Locate every Plasmodium falciparum-infected red blood cell.
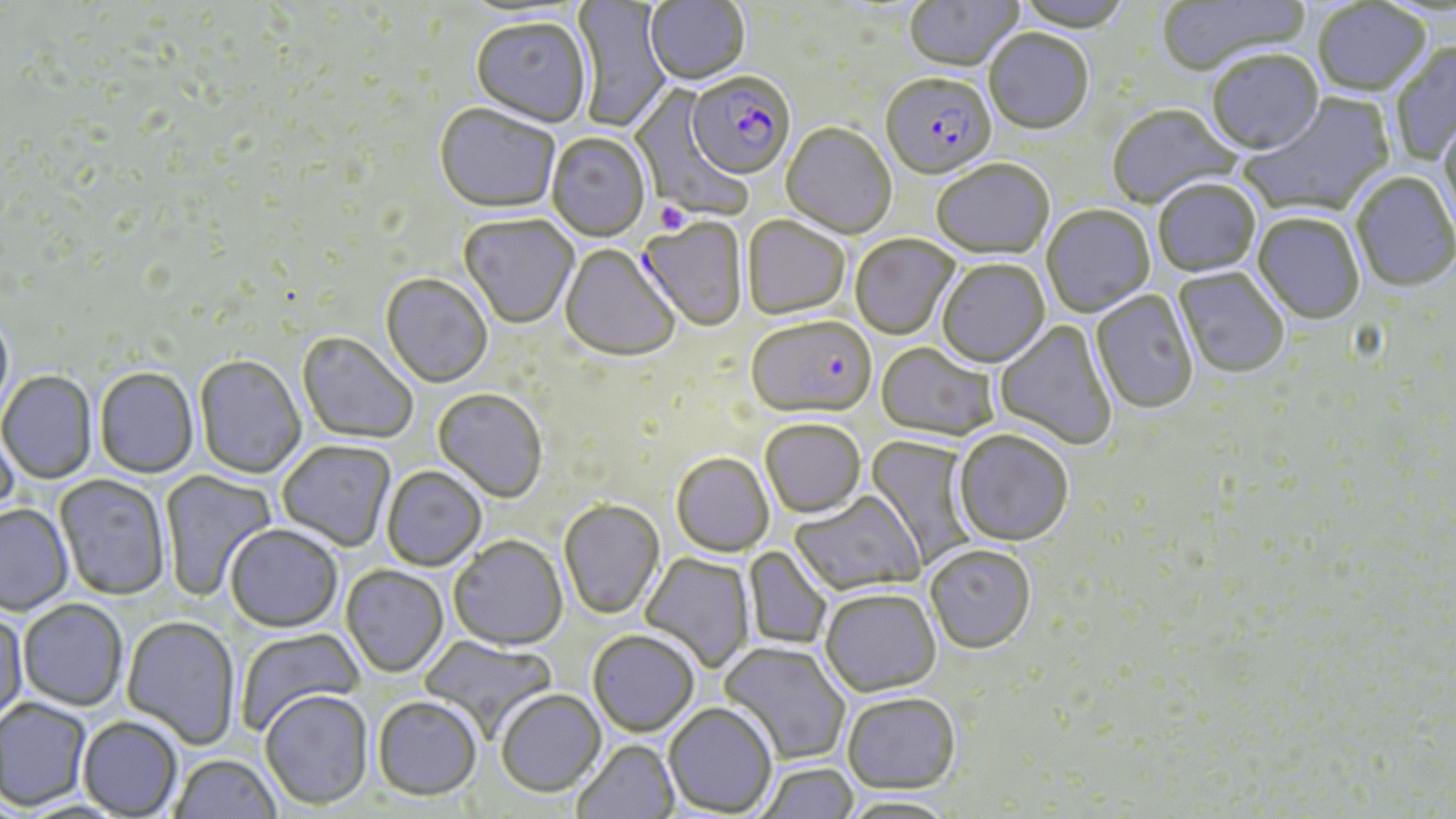
Approximate bounding boxes as (x1, y1, x2, y2) in pixels.
Plasmodium falciparum-infected red blood cells: (686, 74, 796, 182), (881, 75, 996, 182), (747, 318, 876, 422).

slide-level diagnosis = Plasmodium falciparum
stain = May-Grünwald-Giemsa
preparation = thin blood film
modality = optical microscopy
platelet locations = approximate bounding boxes as (x1, y1, x2, y2) in pixels: (652, 203, 686, 232)
magnification = 1000x
image size = 1456×819 pixels
uninfected red blood cell locations = approximate bounding boxes as (x1, y1, x2, y2) in pixels: (644, 0, 751, 87), (904, 0, 1024, 74), (1014, 0, 1133, 35), (1156, 0, 1310, 77), (570, 1, 673, 133), (1313, 2, 1431, 99), (456, 4, 590, 24), (470, 19, 591, 128), (984, 31, 1094, 136), (1391, 40, 1456, 164), (1207, 52, 1324, 158), (628, 83, 753, 221), (1239, 93, 1396, 220), (434, 105, 560, 217), (1108, 106, 1242, 211), (1438, 115, 1456, 238), (781, 124, 896, 239), (547, 134, 650, 243), (932, 161, 1054, 262), (1351, 172, 1455, 294), (1154, 180, 1261, 278), (1043, 206, 1155, 318), (1252, 214, 1365, 326), (458, 215, 578, 330), (742, 218, 850, 321), (637, 219, 748, 333), (850, 236, 960, 341), (559, 246, 680, 364), (937, 260, 1051, 369), (1174, 269, 1289, 380), (380, 274, 492, 389), (1090, 290, 1198, 416), (0, 310, 15, 424), (994, 319, 1117, 451), (297, 333, 418, 445), (876, 344, 998, 443), (194, 355, 306, 479), (94, 368, 199, 478), (0, 371, 97, 484), (433, 389, 547, 503), (760, 420, 865, 519), (0, 426, 19, 526), (953, 432, 1074, 549), (863, 435, 976, 569), (277, 440, 396, 552), (671, 453, 774, 557), (381, 466, 487, 571), (158, 470, 277, 602), (54, 475, 170, 601), (789, 493, 925, 596), (559, 499, 664, 619), (0, 504, 74, 616), (226, 525, 342, 632), (448, 536, 567, 651), (744, 546, 832, 649), (925, 547, 1036, 656), (640, 552, 756, 672), (341, 565, 449, 678), (819, 590, 941, 698), (18, 599, 128, 710), (0, 611, 29, 726), (122, 615, 241, 749), (235, 627, 364, 736), (588, 631, 699, 737), (419, 636, 558, 740), (718, 642, 850, 765), (260, 690, 373, 811), (496, 690, 606, 797), (843, 694, 961, 797), (372, 697, 482, 802), (0, 698, 92, 811), (664, 703, 777, 816), (78, 716, 183, 817), (572, 740, 680, 819), (169, 754, 281, 818), (755, 762, 858, 819), (837, 795, 959, 818)
field of view = one of a larger specimen